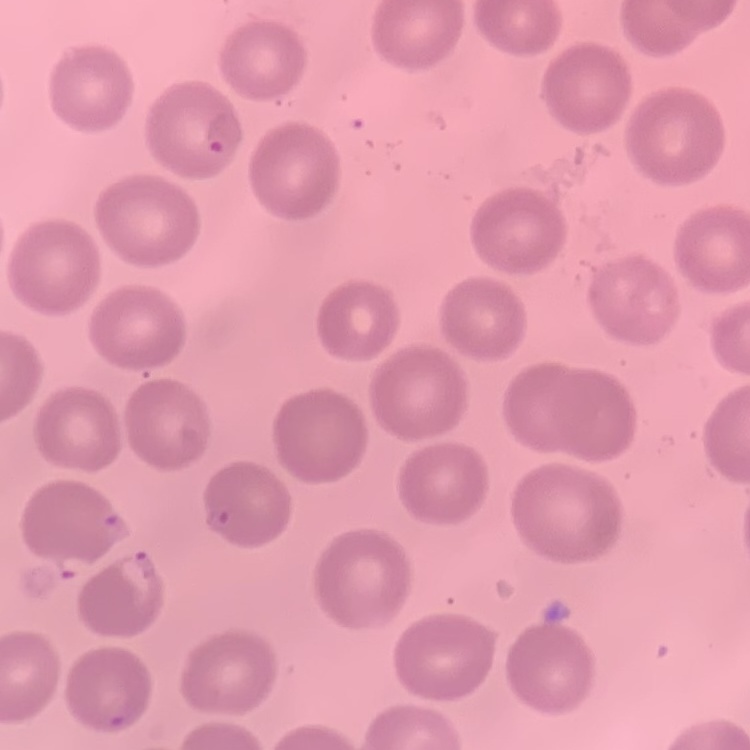

The red blood cells show no rouleaux formation. Field's or Giemsa stain. Thin blood smear. Square crop of a larger photomicrograph.